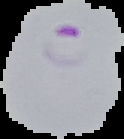 Result: Plasmodium parasites detected. Segmented cell region on a black background. Image is 124×139 pixels. From a thin blood film.